Name the parasite shown.
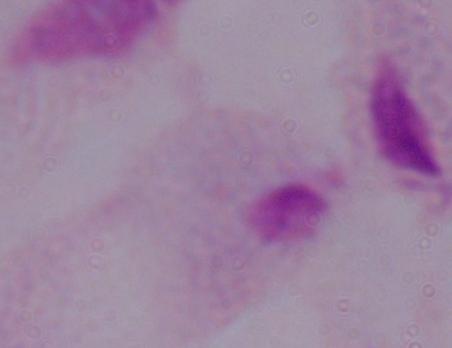
This is a trichomonad.

Captured at 1000x magnification. Micrograph.